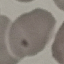

Summary:
  - Result: no malaria parasites seen
  - Capture: smartphone camera at the microscope eyepiece
  - Image type: automatically extracted cell patch, resized to 64 × 64 pixels
  - Stain: Giemsa
  - Preparation: thin blood smear